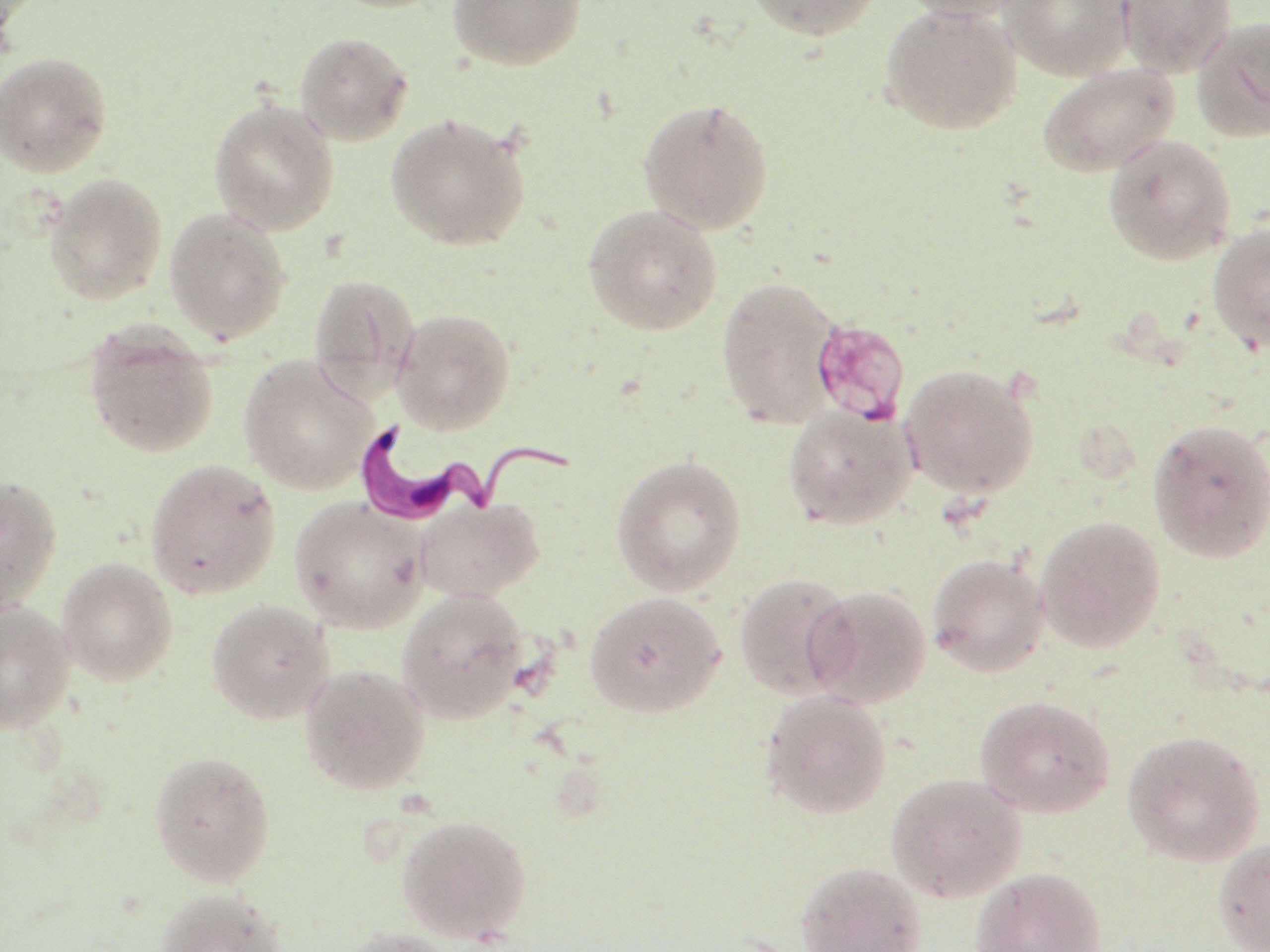
Summary:
  - Coordinate format: approximate bounding boxes as (x1,y1)-(x2,y2) corner pairs in pixels
  - Trypanosoma brucei locations: (345,416)-(580,528)
  - Uninfected red blood cell locations: (447,0)-(587,71), (742,0)-(882,41), (890,0)-(1033,21), (1001,0)-(1133,81), (1117,0)-(1237,79), (878,3)-(1023,137), (1191,14)-(1270,143), (294,31)-(413,146), (0,50)-(113,178), (1036,61)-(1181,177), (208,97)-(340,236), (637,97)-(775,235), (384,112)-(532,251), (1102,133)-(1237,267), (43,172)-(168,305), (582,203)-(723,335), (163,206)-(291,346), (1206,222)-(1270,355), (307,273)-(419,399), (715,275)-(842,429), (392,307)-(516,435), (83,323)-(219,459), (238,355)-(379,495), (900,363)-(1040,500), (781,406)-(917,531), (1147,417)-(1270,563), (610,453)-(748,596), (144,457)-(282,600), (0,475)-(62,616), (289,496)-(430,634), (414,498)-(544,602), (1034,515)-(1166,653), (926,553)-(1050,677), (56,556)-(178,687), (733,572)-(857,700), (805,585)-(932,709), (396,587)-(532,726), (584,590)-(727,719), (205,597)-(335,724), (0,600)-(76,733), (298,663)-(431,796), (759,690)-(892,820), (974,694)-(1117,819), (1122,728)-(1267,867), (148,749)-(276,888), (885,771)-(1027,902), (396,812)-(533,944), (1213,837)-(1270,952), (795,860)-(928,952), (971,866)-(1108,952), (154,887)-(287,951), (338,926)-(462,952)
  - Slide-level diagnosis: Trypanosoma brucei
  - Preparation: thin blood smear
  - Modality: light microscopy
  - Field of view: one of a larger specimen
  - Image size: 1270×952 pixels
  - Magnification: 1000x
  - Stain: May-Grünwald-Giemsa